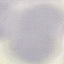
result = no malaria parasites seen
stain = Giemsa
capture = smartphone through the microscope eyepiece
preparation = thin blood film
image type = automatically extracted cell patch, resized to 64 × 64 pixels